Name the blood parasite species.
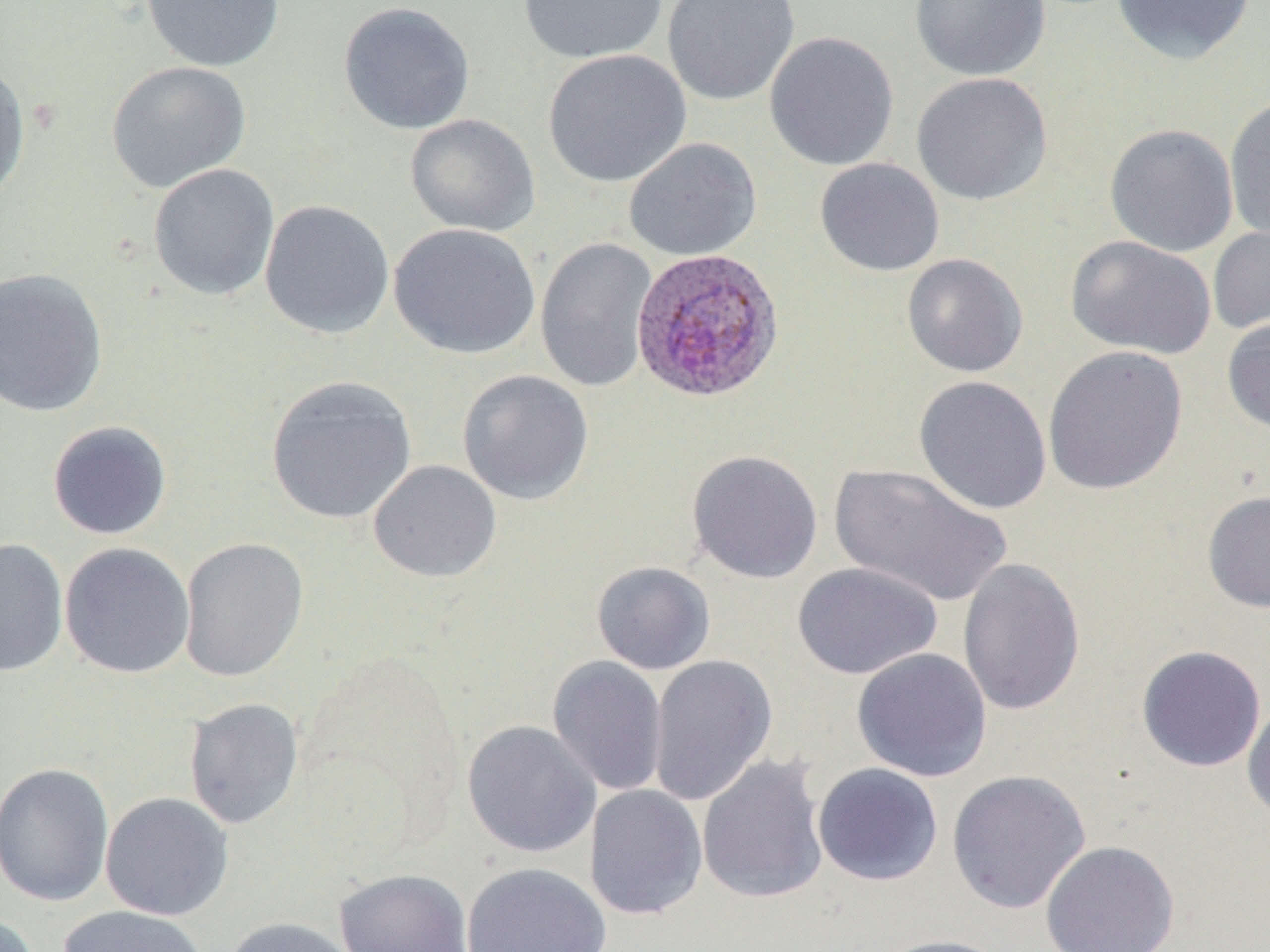
Plasmodium ovale.

Approximate bounding boxes as [x1, y1, x2, y2] in pixels. Plasmodium ovale-infected red blood cell locations: [631, 246, 784, 403]. Uninfected red blood cell locations: [140, 0, 284, 72], [516, 0, 668, 64], [662, 0, 800, 106], [909, 0, 1050, 82], [1110, 0, 1257, 65], [338, 2, 476, 135], [764, 30, 899, 171], [542, 49, 691, 188], [0, 61, 31, 203], [106, 61, 251, 194], [911, 71, 1053, 206], [1224, 95, 1270, 244], [404, 114, 540, 237], [1104, 123, 1239, 256], [623, 137, 762, 261], [814, 157, 945, 277], [148, 164, 280, 301], [259, 200, 394, 339], [388, 223, 541, 359], [1207, 225, 1270, 337], [1065, 235, 1217, 360], [535, 237, 657, 392], [902, 253, 1029, 378], [0, 267, 109, 418], [1222, 317, 1270, 434], [1043, 345, 1188, 495], [457, 369, 594, 506], [265, 375, 417, 524], [913, 375, 1053, 515], [47, 420, 173, 540], [687, 449, 823, 584], [368, 459, 501, 583], [828, 463, 1013, 608], [1202, 489, 1270, 613], [178, 537, 309, 682], [0, 538, 68, 676], [59, 542, 195, 679], [957, 558, 1086, 716], [591, 560, 716, 675], [792, 562, 943, 680], [1136, 645, 1266, 772], [852, 648, 992, 782], [647, 654, 778, 807], [546, 655, 669, 796], [183, 697, 304, 830], [1242, 697, 1270, 825], [461, 719, 601, 858], [696, 754, 829, 905], [0, 761, 115, 908], [812, 763, 944, 886], [946, 769, 1092, 914], [584, 784, 708, 921], [100, 792, 234, 921], [1040, 840, 1180, 952], [461, 862, 612, 952], [334, 868, 474, 952], [55, 905, 209, 952], [0, 914, 40, 952], [220, 917, 360, 952], [874, 934, 1014, 952]. Thin blood smear. May-Grünwald-Giemsa-stained preparation. Optical microscopy. 1000x magnification. Single field of view. Image is 1270×952 pixels.